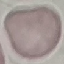

Summary:
  - Result: negative for malaria parasites
  - Image type: automatically extracted cell patch, resized to 64 × 64 pixels
  - Capture: smartphone through the microscope eyepiece
  - Stain: Giemsa
  - Preparation: thin blood smear